Identify the preparation type.
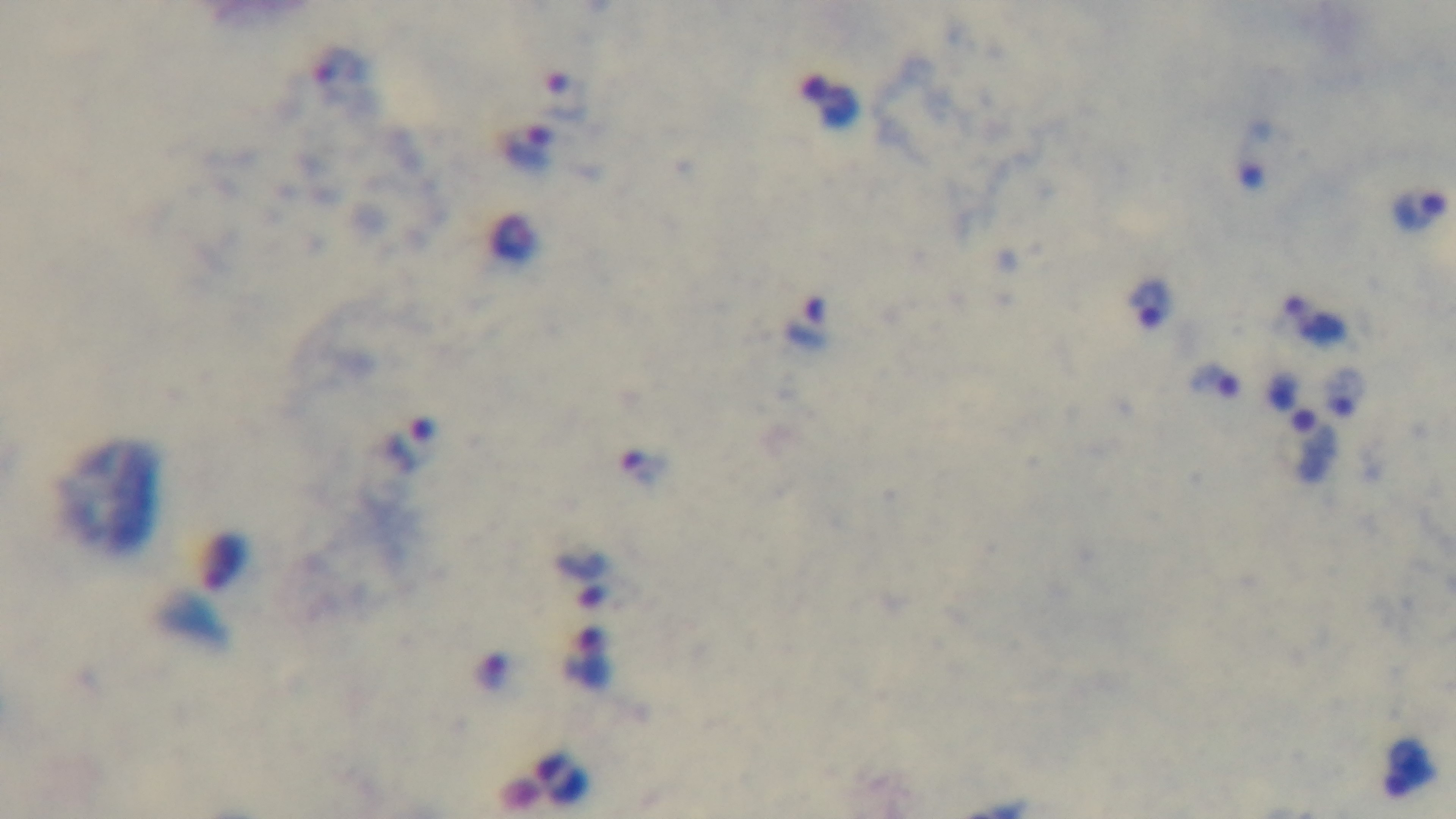

A thick smear.

Summary:
  - Capture: mounted 4K digital camera
  - Objective: 100x oil immersion
  - Stain: Giemsa
  - Modality: light microscopy
  - Malaria status: positive
  - Field of view: single